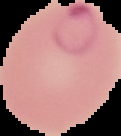

From a thin blood film. Result: Plasmodium parasites identified. Image is 121×136 pixels. The area outside the segmented cell region is set to black.